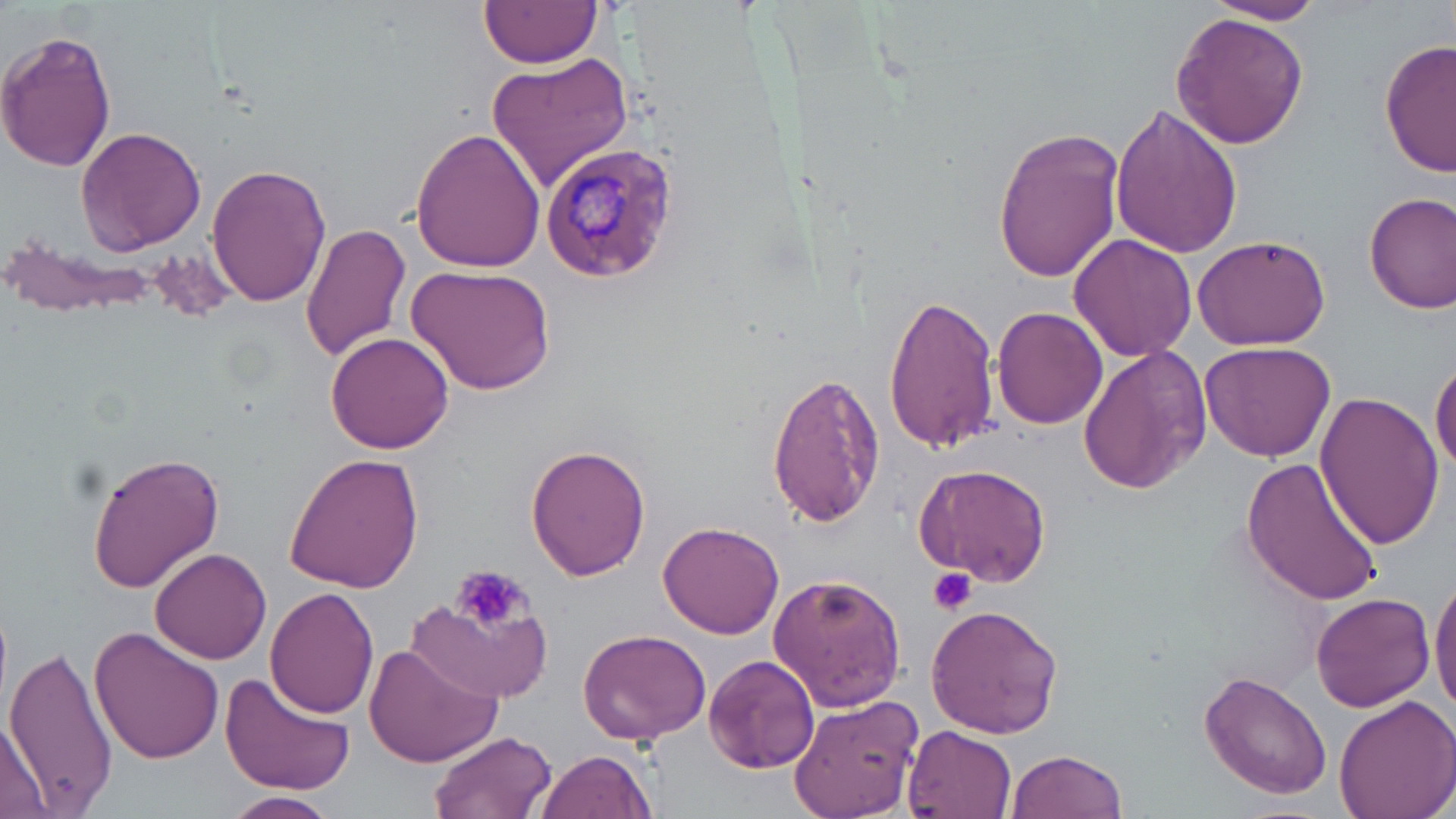

Plasmodium malariae-infected red blood cell locations = approximate bounding boxes as (x1, y1, x2, y2) in pixels: (538, 142, 680, 284)
slide-level diagnosis = Plasmodium malariae
uninfected red blood cell locations = approximate bounding boxes as (x1, y1, x2, y2) in pixels: (480, 0, 602, 69), (1206, 0, 1330, 25), (1171, 14, 1310, 147), (0, 28, 118, 175), (1379, 39, 1455, 180), (485, 50, 634, 190), (1108, 102, 1242, 259), (994, 125, 1125, 283), (75, 126, 207, 254), (410, 127, 546, 273), (206, 161, 327, 308), (1365, 192, 1456, 314), (300, 222, 411, 361), (1069, 234, 1196, 362), (1193, 234, 1331, 349), (6, 237, 163, 322), (408, 262, 557, 397), (883, 292, 1001, 454), (990, 306, 1107, 429), (325, 332, 457, 456), (1200, 341, 1336, 462), (1078, 346, 1212, 495), (1431, 357, 1456, 477), (767, 370, 886, 529), (1313, 392, 1445, 549), (525, 444, 651, 580), (86, 451, 224, 591), (286, 451, 426, 594), (1240, 456, 1386, 607), (914, 462, 1053, 589), (659, 522, 785, 639), (150, 545, 271, 664), (119, 556, 240, 735), (768, 571, 907, 711), (1429, 572, 1456, 716), (264, 586, 380, 718), (1310, 592, 1438, 712), (408, 600, 555, 704), (925, 603, 1064, 739), (90, 624, 225, 765), (579, 629, 713, 747), (362, 643, 502, 770), (4, 645, 118, 815), (703, 653, 819, 773), (1199, 668, 1332, 797), (219, 672, 355, 796), (790, 691, 924, 819), (1330, 695, 1456, 819), (1, 715, 50, 817), (902, 723, 1017, 819), (429, 729, 556, 819), (533, 749, 656, 819), (1006, 749, 1127, 819), (228, 791, 338, 817)
platelet locations = approximate bounding boxes as (x1, y1, x2, y2) in pixels: (452, 565, 530, 634), (926, 568, 979, 618)
image size = 1456×819 pixels
stain = May-Grünwald-Giemsa
magnification = 1000x
preparation = thin blood smear
field of view = single
modality = optical microscopy